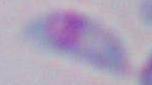

Toxoplasma gondii is seen. 1000x magnification. Micrograph.